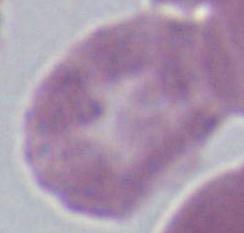

Summary:
  - Modality: micrograph
  - Magnification: 1000x
  - Identification: red blood cell